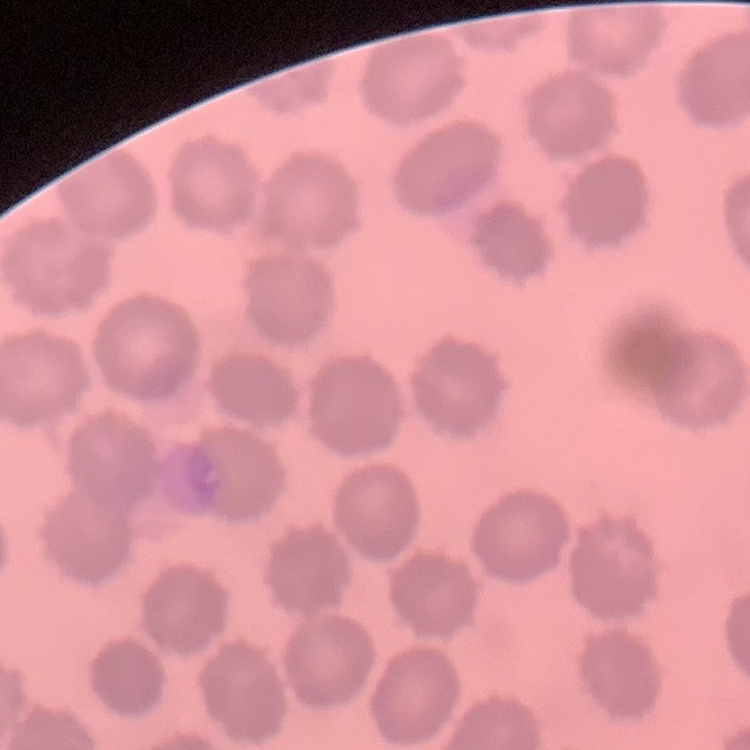 The red blood cells exhibit no rouleaux formation. Stained with either Field's or Giemsa. Thin blood smear. One tile cut from a larger photomicrograph.